Classify this cell by malaria status.
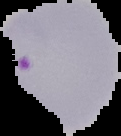
Parasitized.

Image is 121×136 pixels. From a thin blood smear. Segmented cell region on a black background.